Name the blood parasite species.
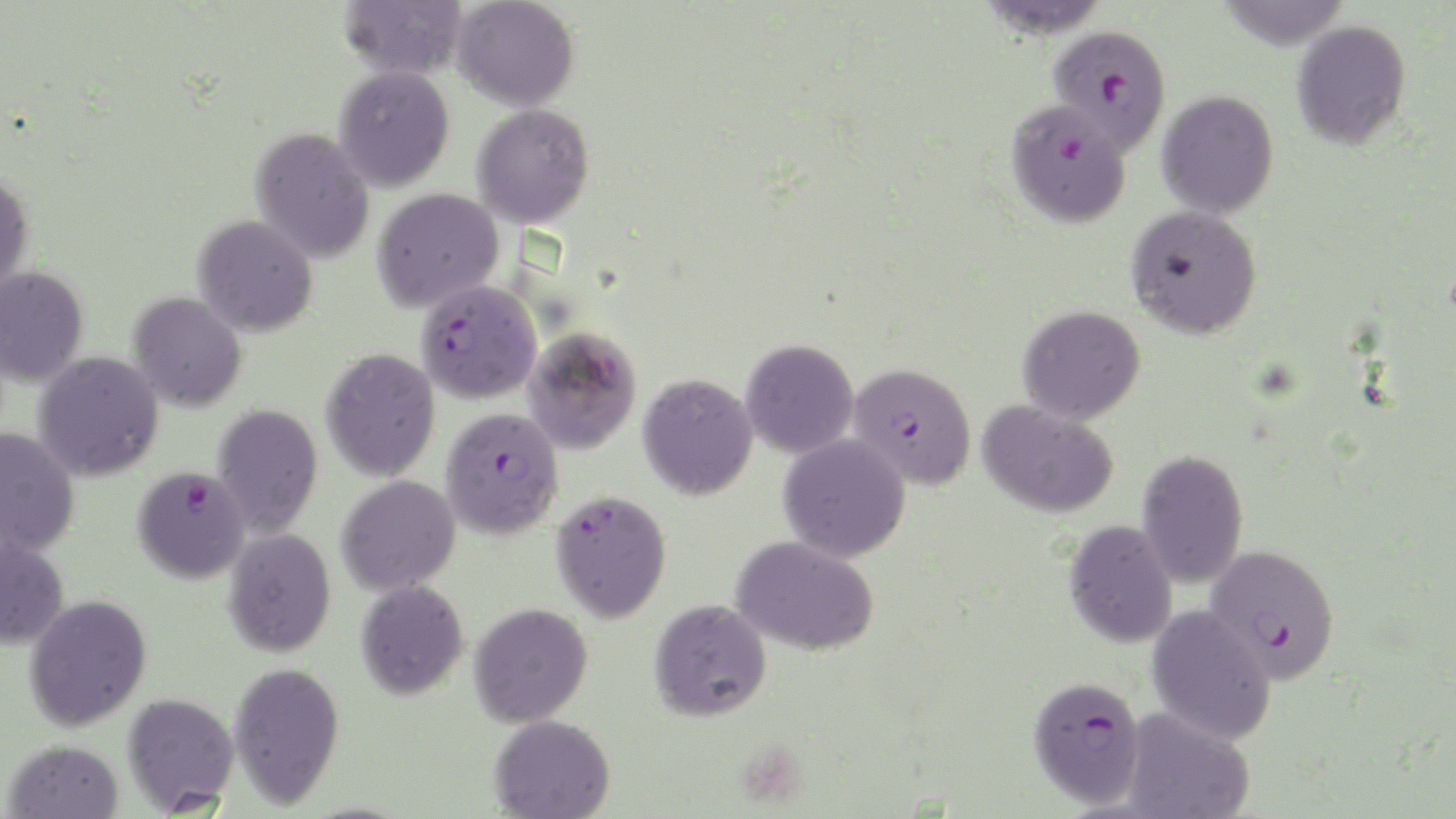

Plasmodium falciparum.

Approximate bounding boxes as named x1/y1/x2/y2 corners in pixels. Plasmodium falciparum-infected red blood cell locations: (x1=1047, y1=25, x2=1172, y2=152), (x1=1005, y1=100, x2=1132, y2=230), (x1=415, y1=279, x2=542, y2=404), (x1=847, y1=362, x2=977, y2=488), (x1=440, y1=406, x2=564, y2=539), (x1=132, y1=465, x2=250, y2=583), (x1=550, y1=489, x2=672, y2=623), (x1=1204, y1=543, x2=1340, y2=682), (x1=1027, y1=674, x2=1146, y2=808). Uninfected red blood cell locations: (x1=338, y1=0, x2=468, y2=80), (x1=452, y1=0, x2=580, y2=112), (x1=1291, y1=19, x2=1412, y2=150), (x1=333, y1=65, x2=455, y2=191), (x1=1156, y1=90, x2=1279, y2=219), (x1=471, y1=104, x2=595, y2=228), (x1=250, y1=127, x2=375, y2=263), (x1=0, y1=171, x2=35, y2=296), (x1=372, y1=187, x2=504, y2=313), (x1=1126, y1=205, x2=1263, y2=339), (x1=192, y1=215, x2=319, y2=337), (x1=0, y1=266, x2=89, y2=387), (x1=127, y1=291, x2=247, y2=411), (x1=1018, y1=305, x2=1146, y2=424), (x1=522, y1=326, x2=642, y2=455), (x1=740, y1=338, x2=859, y2=459), (x1=320, y1=348, x2=440, y2=481), (x1=33, y1=352, x2=164, y2=481), (x1=637, y1=372, x2=758, y2=500), (x1=977, y1=399, x2=1119, y2=518), (x1=212, y1=403, x2=323, y2=538), (x1=0, y1=428, x2=79, y2=556), (x1=777, y1=433, x2=911, y2=561), (x1=1136, y1=449, x2=1249, y2=589), (x1=336, y1=475, x2=460, y2=596), (x1=1063, y1=521, x2=1178, y2=648), (x1=223, y1=528, x2=336, y2=657), (x1=0, y1=534, x2=70, y2=649), (x1=730, y1=535, x2=880, y2=656), (x1=355, y1=580, x2=468, y2=700), (x1=24, y1=594, x2=152, y2=730), (x1=648, y1=598, x2=772, y2=722), (x1=469, y1=602, x2=593, y2=726), (x1=1145, y1=604, x2=1277, y2=745), (x1=228, y1=661, x2=345, y2=807), (x1=122, y1=692, x2=240, y2=814), (x1=1120, y1=708, x2=1255, y2=819), (x1=489, y1=714, x2=616, y2=819), (x1=3, y1=738, x2=124, y2=818). Thin blood film. Light microscopy. Image is 1456×819 pixels. 1000x magnification. One field of a larger specimen. May-Grünwald-Giemsa-stained preparation.